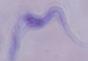

Summary:
  - Modality: photomicrograph
  - Magnification: 1000x
  - Identification: trypanosome